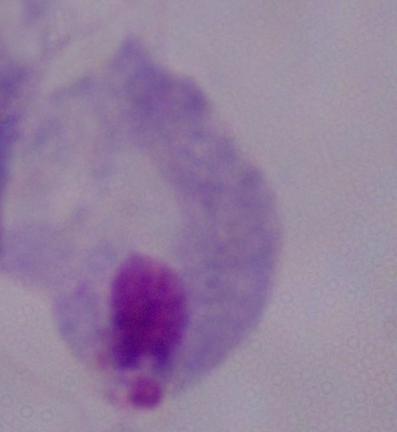

Summary:
  - Modality: micrograph
  - Identification: trichomonad
  - Magnification: 1000x